Give the position of every Plasmodium parasite.
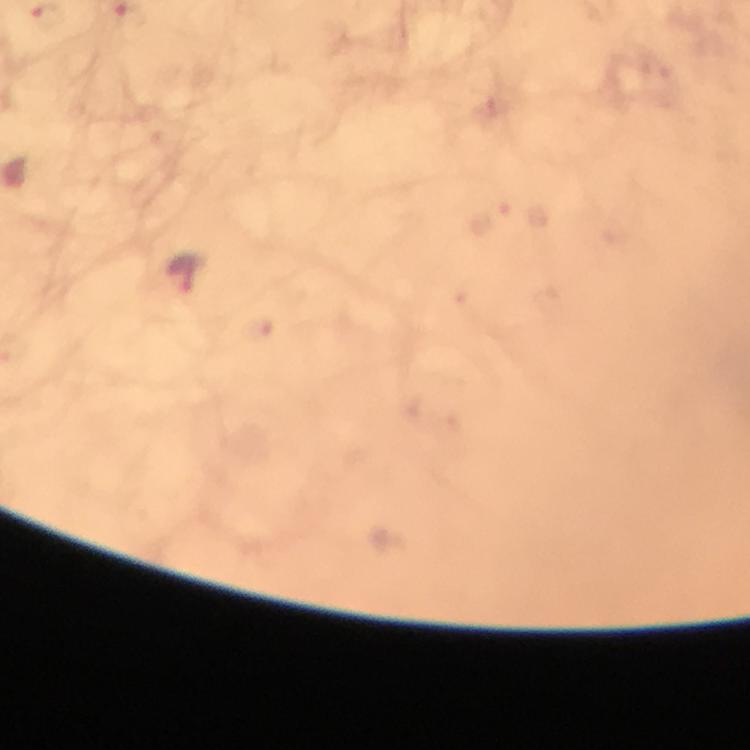

Approximate object centers, in pixels from the top-left corner.
Plasmodium parasites: (x=45, y=18), (x=185, y=275).

preparation = thick smear
immersion oil = applied
magnification = 100x
capture = smartphone mounted on the microscope
image size = 750×750 pixels
cropped from = a single field of view
context = from a diagnostic examination for malaria
stain = Giemsa